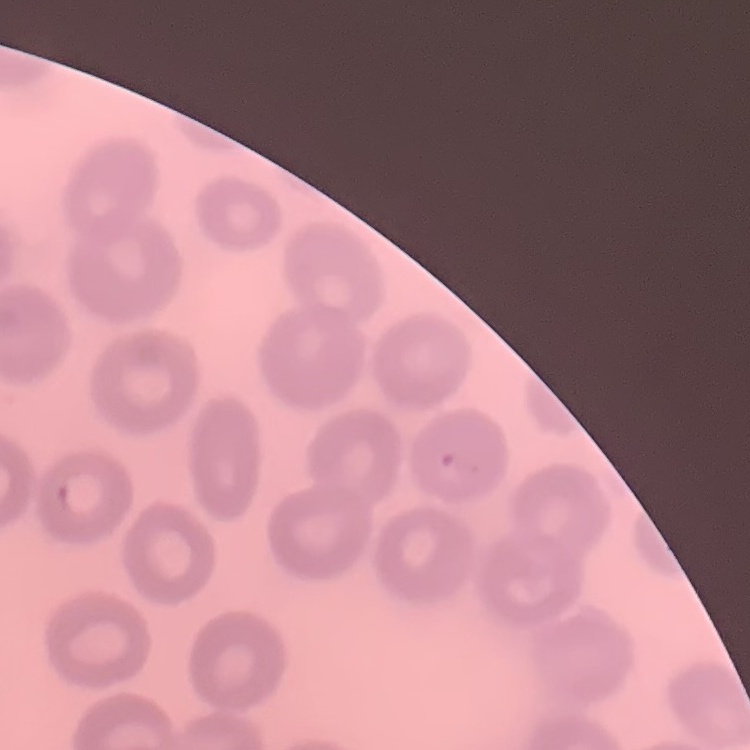
erythrocyte morphology = no rouleaux formation
stain = Field's or Giemsa
preparation = thin peripheral smear
image type = square crop of a larger photomicrograph